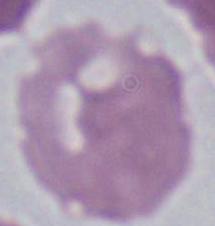 Captured at 1000x magnification. An erythrocyte is shown. Micrograph.